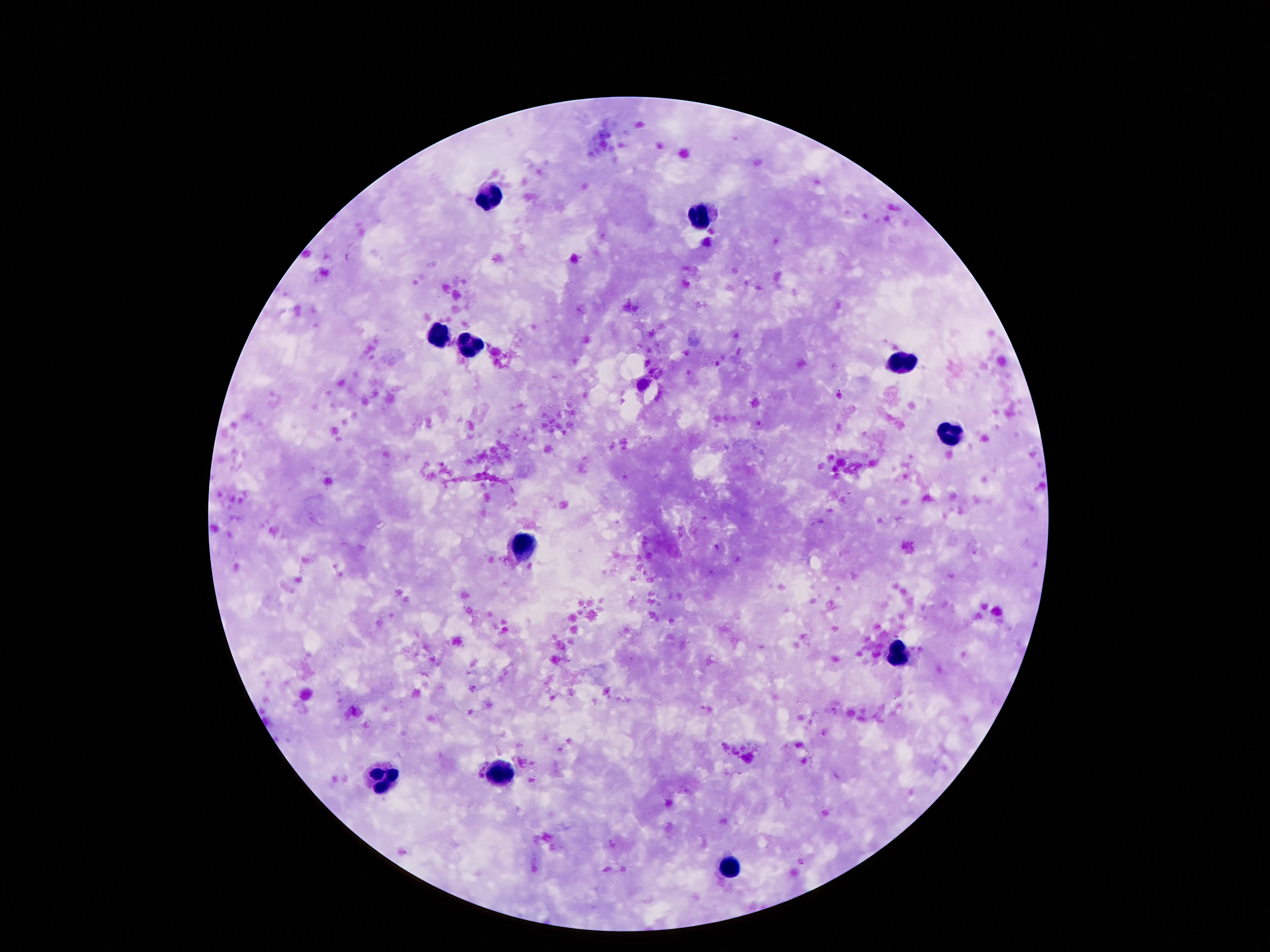

field of view = single
image size = 1270×952 pixels
stain = Giemsa
magnification = 100x
leukocyte locations = approximate centers as (x, y) in pixels: (490, 195), (699, 212), (441, 334), (471, 345), (902, 361), (947, 433), (521, 543), (894, 652), (500, 774), (381, 781), (732, 871)
capture = smartphone camera through the microscope eyepiece
preparation = thick blood smear
patient malaria status = uninfected